Name the cell type shown.
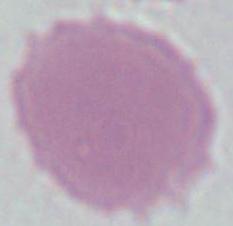

An erythrocyte.

Summary:
  - Magnification: 1000x
  - Modality: micrograph